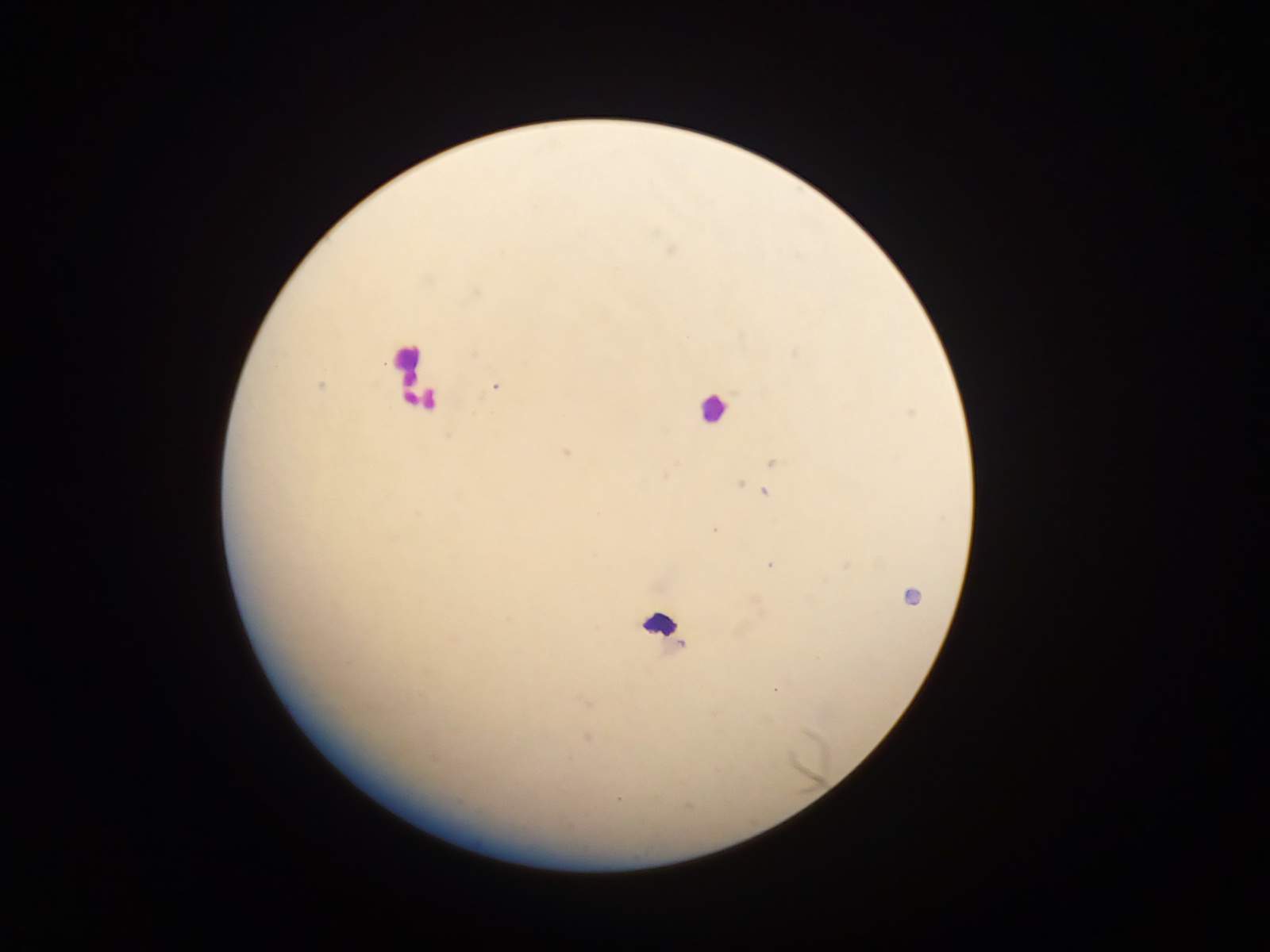

Approximate centers as x y in pixels. Leukocyte locations: 409 365; 713 407; 661 623. Malaria parasite locations: 320 386; 495 387; 566 452; 772 462; 739 483; 765 494; 714 530; 770 565; 910 597; 682 645; 775 689; 585 702; 587 738; 618 800. Collected in Ghana. Mobile-phone photograph taken through the microscope. One field of view. Image is 1270×952 pixels. Thick blood film.